Describe the morphology of the red blood cells.
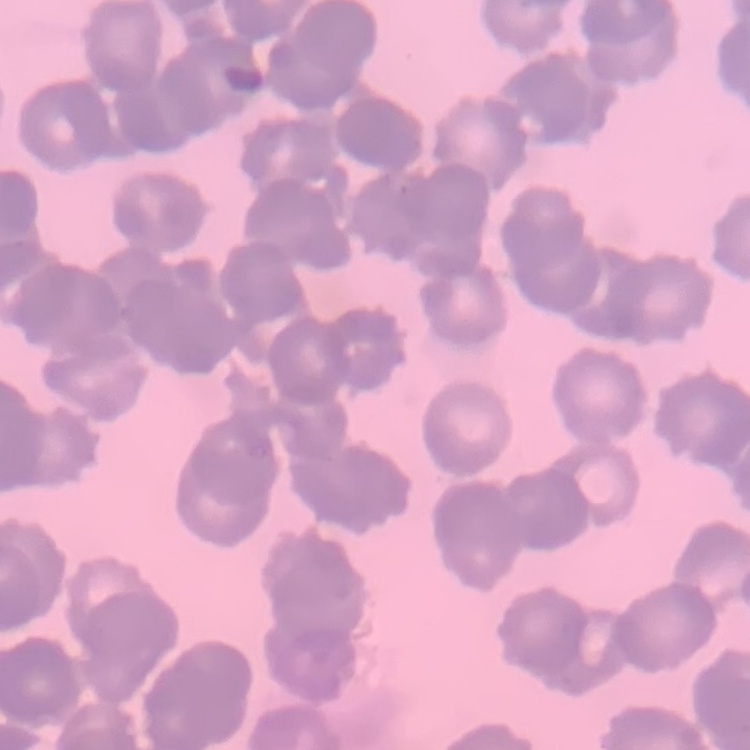
Rouleaux formation.

Summary:
  - Preparation: thin blood film
  - Image type: square crop of a larger photomicrograph
  - Stain: Field's or Giemsa